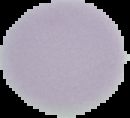

From a thin blood film. Segmented cell region on a black background. Image is 130×118 pixels. Malaria status: uninfected.